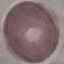 Malaria status: uninfected. Cell patch, automatically extracted from a larger field of view and resized to 64 × 64 pixels. Acquired by smartphone through the microscope eyepiece. Thin blood film. Giemsa-stained preparation.